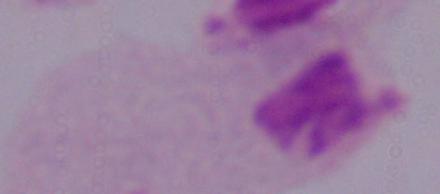

magnification = 1000x
modality = photomicrograph
identification = trichomonad